Point out leukocytes.
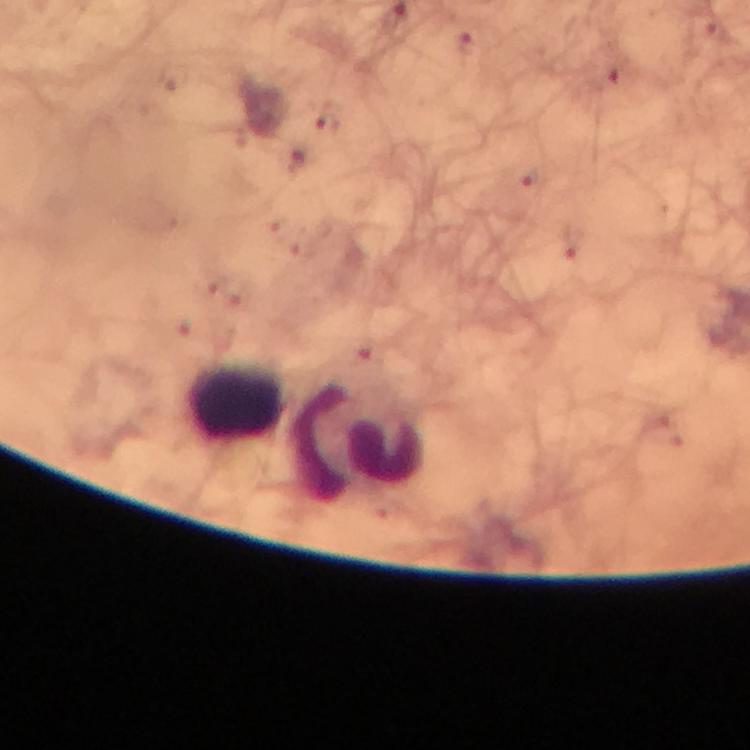
Approximate centers as (x, y) in pixels.
Leukocytes: (236, 403), (358, 438).

Summary:
  - Stain: Giemsa
  - Malaria parasites: none seen
  - Immersion oil: used
  - Image size: 750×750 pixels
  - Capture: smartphone mounted on the microscope
  - Preparation: thick blood film
  - Magnification: 100x
  - Context: from a diagnostic examination for malaria
  - Cropped from: a single field of view